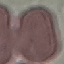
{
  "malaria_status": "uninfected",
  "preparation": "thin blood smear",
  "stain": "Giemsa",
  "image_type": "cell patch, automatically extracted from a larger field of view and resized to 64 × 64 pixels",
  "capture": "smartphone camera at the microscope eyepiece"
}